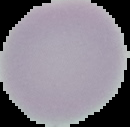
image size = 130×127 pixels
preparation = thin blood film
result = negative for Plasmodium parasites
image type = cell region segmented out of the field of view; surrounding area masked to black